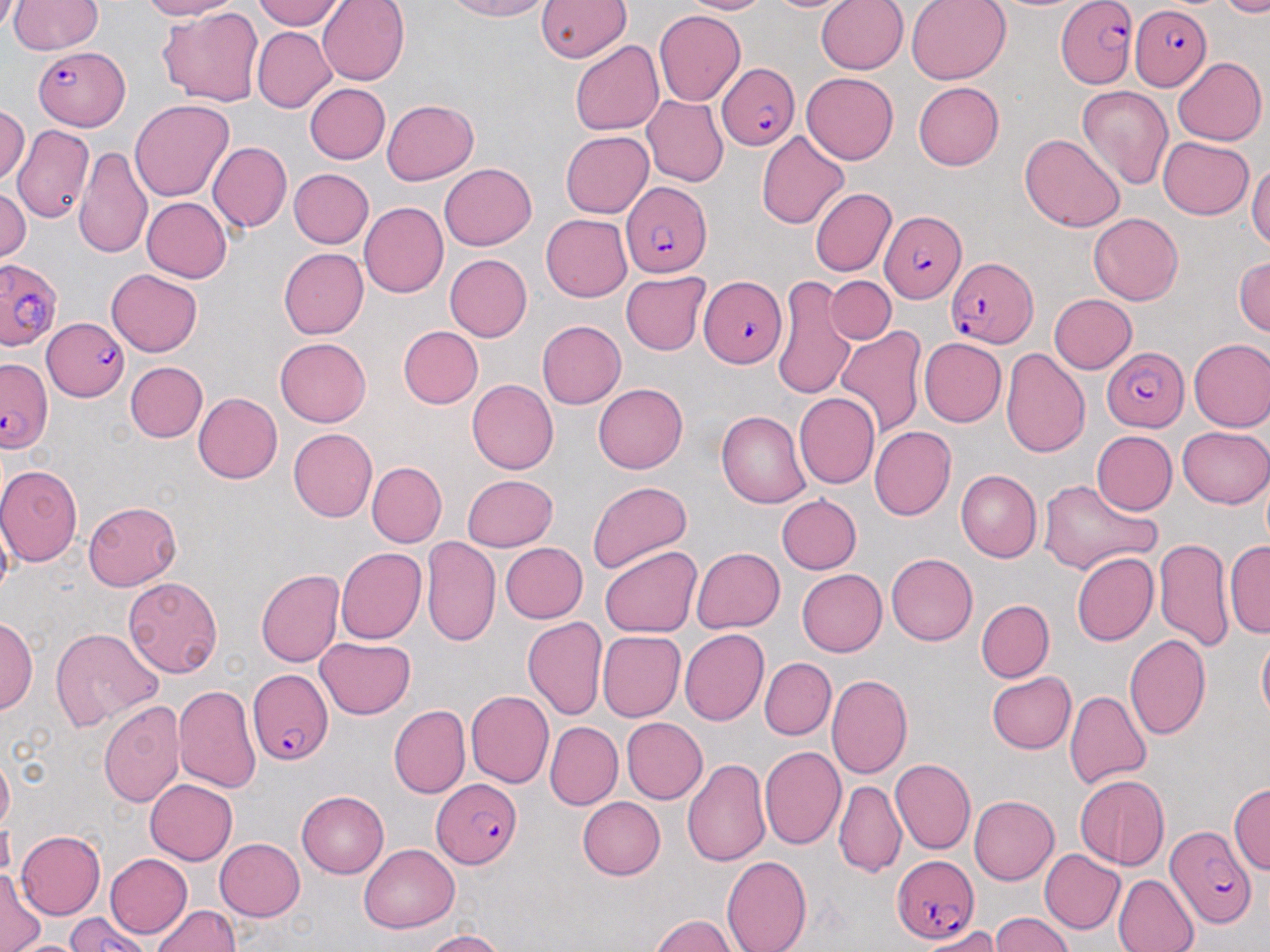
slide-level diagnosis = Plasmodium falciparum
preparation = thin blood smear
uninfected red blood cell locations = approximate bounding boxes as [x1, y1, x2, y2] in pixels: [9, 0, 103, 54], [134, 0, 237, 20], [251, 0, 346, 29], [315, 0, 409, 86], [441, 0, 559, 21], [536, 0, 628, 64], [677, 0, 773, 16], [759, 0, 851, 14], [816, 0, 909, 74], [906, 0, 1010, 84], [1223, 0, 1270, 15], [157, 6, 264, 106], [655, 11, 744, 105], [251, 26, 337, 112], [570, 40, 663, 136], [1171, 56, 1265, 145], [800, 73, 898, 165], [913, 81, 1003, 170], [304, 83, 391, 165], [1075, 85, 1174, 192], [642, 97, 728, 185], [129, 99, 234, 201], [383, 100, 479, 184], [1, 105, 30, 182], [555, 113, 715, 202], [16, 124, 94, 223], [560, 131, 653, 216], [757, 131, 849, 230], [1021, 133, 1125, 232], [1158, 139, 1255, 219], [207, 142, 291, 233], [74, 146, 154, 257], [1250, 155, 1270, 257], [439, 163, 536, 250], [288, 169, 374, 248], [0, 185, 29, 265], [811, 187, 896, 276], [141, 197, 231, 282], [359, 202, 447, 298], [541, 211, 635, 302], [1089, 212, 1184, 303], [278, 248, 369, 339], [1233, 253, 1269, 338], [442, 254, 531, 341], [106, 270, 203, 356], [620, 272, 709, 355], [828, 275, 895, 345], [772, 278, 863, 397], [1047, 294, 1135, 374], [535, 320, 624, 409], [837, 325, 926, 438], [399, 326, 483, 408], [275, 337, 372, 426], [919, 338, 1005, 426], [1188, 338, 1270, 431], [1000, 347, 1090, 457], [125, 360, 207, 442], [467, 379, 558, 474], [593, 383, 687, 473], [194, 392, 282, 484], [793, 393, 878, 488], [716, 411, 811, 507], [1179, 424, 1270, 507], [869, 426, 955, 521], [288, 428, 377, 521], [1089, 430, 1177, 517], [366, 462, 446, 548], [0, 465, 81, 566], [956, 469, 1041, 560], [463, 474, 558, 550], [1037, 478, 1160, 574], [586, 480, 691, 574], [774, 495, 861, 575], [82, 500, 184, 589], [421, 536, 501, 646], [1153, 536, 1233, 651], [1225, 539, 1270, 638], [1179, 540, 1270, 645], [499, 542, 588, 623], [335, 546, 424, 642], [600, 546, 701, 637], [691, 546, 786, 632], [1071, 551, 1158, 645], [884, 553, 976, 645], [256, 569, 343, 666], [798, 569, 887, 656], [124, 577, 223, 678], [975, 599, 1053, 681], [522, 614, 608, 719], [1, 618, 37, 716], [49, 627, 163, 729], [678, 628, 769, 727], [596, 630, 685, 722], [1123, 633, 1211, 742], [1256, 634, 1270, 729], [316, 637, 417, 718], [761, 657, 835, 739], [986, 671, 1076, 753], [826, 674, 911, 780], [174, 682, 262, 795], [468, 690, 556, 787], [1065, 690, 1152, 790], [100, 700, 187, 809], [390, 705, 471, 799], [619, 717, 706, 805], [546, 721, 622, 807], [759, 745, 845, 850], [0, 756, 12, 831], [682, 756, 770, 867], [889, 757, 974, 856], [1073, 773, 1171, 869], [144, 778, 236, 865], [835, 781, 905, 876], [1228, 782, 1269, 876], [295, 790, 388, 877], [970, 796, 1058, 884], [578, 797, 665, 879], [14, 831, 103, 919], [0, 837, 66, 937], [215, 837, 306, 920], [358, 844, 459, 934], [1041, 850, 1125, 935], [105, 852, 193, 938], [720, 856, 812, 951], [0, 867, 44, 952], [1113, 875, 1199, 952], [152, 903, 241, 952], [648, 912, 740, 952], [991, 914, 1074, 952], [919, 928, 1006, 950], [416, 930, 512, 951], [13, 935, 80, 952]
stain = May-Grünwald-Giemsa
modality = light microscopy
magnification = 1000x
Plasmodium falciparum-infected red blood cell locations = approximate bounding boxes as [x1, y1, x2, y2] in pixels: [1056, 0, 1136, 87], [1130, 4, 1210, 90], [35, 45, 132, 128], [718, 64, 800, 152], [621, 181, 712, 275], [880, 207, 967, 303], [944, 253, 1037, 348], [1, 257, 65, 355], [699, 275, 788, 366], [44, 318, 126, 400], [1102, 347, 1190, 431], [0, 357, 54, 452], [248, 665, 332, 763], [431, 779, 524, 867], [1164, 826, 1254, 928], [888, 855, 976, 944], [63, 915, 153, 952]
field of view = single
image size = 1270×952 pixels